Classify this cell by malaria status.
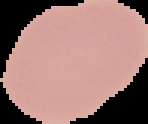
It is uninfected.

Image is 148×124 pixels. The area outside the segmented cell region is set to black. From a thin blood smear.